Outline each uninfected red blood cell.
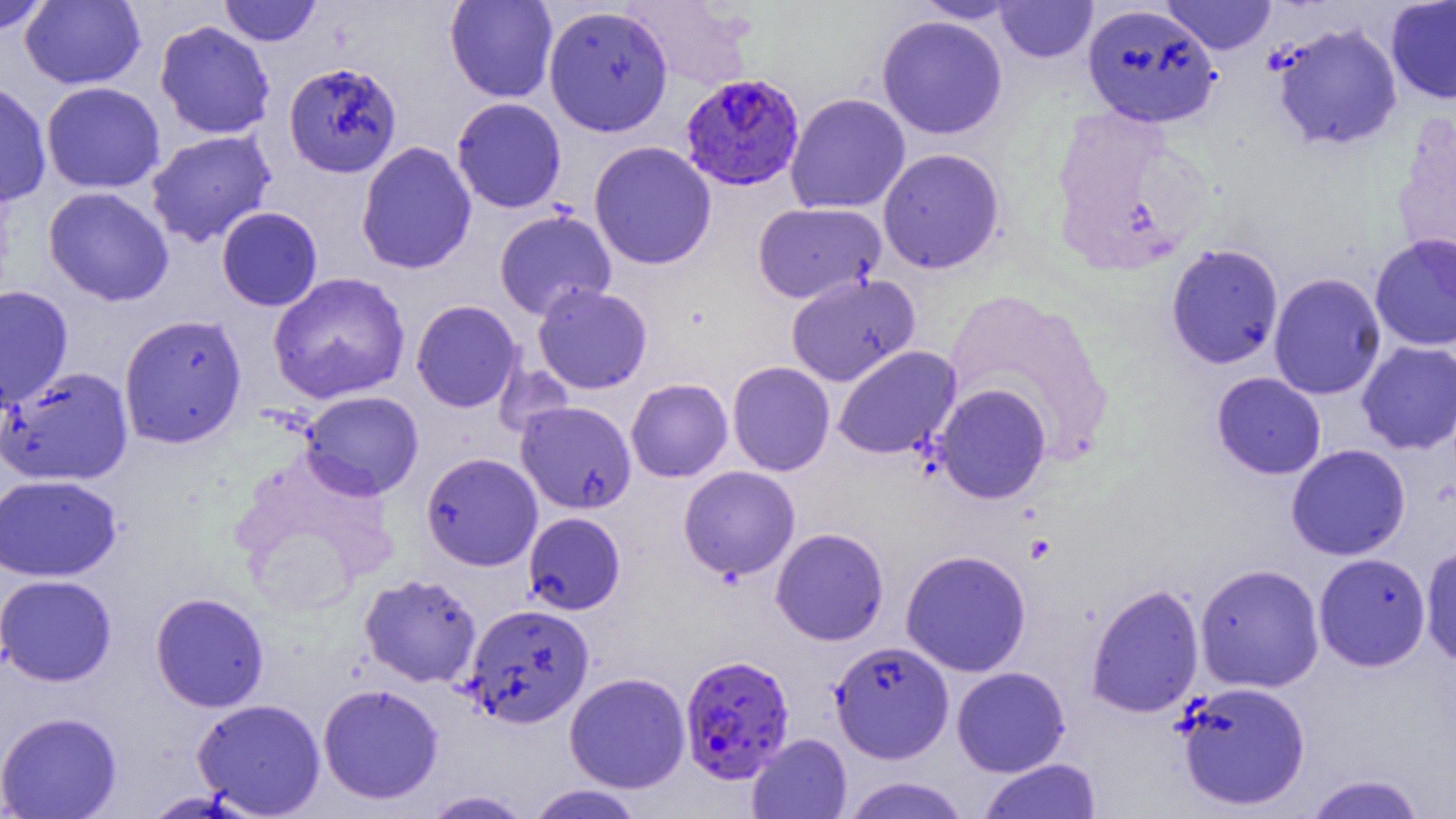
Approximate bounding boxes as [x1, y1, x2, y2] in pixels.
Uninfected red blood cells: [0, 0, 53, 36], [219, 0, 322, 46], [444, 0, 558, 103], [623, 0, 757, 92], [1161, 0, 1277, 55], [1385, 0, 1456, 105], [20, 1, 145, 89], [913, 1, 1023, 23], [994, 1, 1098, 63], [1082, 4, 1220, 128], [543, 5, 673, 137], [877, 15, 1008, 140], [154, 20, 275, 140], [1271, 23, 1403, 151], [283, 62, 403, 178], [0, 79, 52, 206], [41, 81, 165, 194], [785, 93, 910, 214], [451, 97, 567, 213], [1392, 115, 1456, 274], [146, 130, 277, 247], [356, 141, 477, 275], [589, 141, 716, 270], [878, 148, 1005, 274], [43, 187, 174, 306], [752, 201, 885, 303], [216, 207, 322, 311], [494, 209, 616, 321], [1369, 232, 1456, 351], [1165, 243, 1284, 370], [268, 272, 411, 404], [786, 272, 920, 386], [1268, 273, 1386, 400], [532, 283, 652, 394], [0, 285, 73, 410], [942, 288, 1115, 467], [411, 300, 523, 413], [119, 314, 247, 448], [1356, 341, 1456, 454], [833, 346, 962, 459], [727, 361, 835, 476], [0, 366, 133, 486], [1211, 372, 1327, 480], [626, 378, 732, 482], [933, 383, 1051, 504], [301, 390, 423, 500], [516, 401, 637, 514], [1286, 444, 1411, 561], [230, 449, 400, 611], [421, 452, 543, 571], [678, 465, 800, 581], [0, 474, 122, 581], [523, 512, 625, 615], [771, 527, 889, 646], [1420, 543, 1456, 667], [900, 549, 1031, 677], [1314, 553, 1431, 671], [1194, 563, 1324, 693], [0, 574, 117, 687], [359, 574, 482, 687], [1085, 583, 1204, 719], [150, 592, 269, 712], [464, 604, 595, 728], [829, 641, 954, 763], [951, 666, 1070, 776], [564, 672, 690, 793], [1175, 680, 1311, 811], [318, 683, 443, 804], [192, 698, 326, 817], [0, 711, 122, 818], [747, 733, 852, 818], [978, 758, 1102, 819], [1301, 773, 1428, 818], [840, 776, 971, 819], [526, 784, 645, 819], [420, 789, 534, 818].

slide_level_diagnosis: Plasmodium falciparum
magnification: 1000x
field_of_view: single
preparation: thin blood smear
plasmodium_falciparum_infected_red_blood_cell_locations: 'approximate bounding boxes as [x1, y1, x2, y2] in pixels: [680, 73, 805, 191], [680, 654, 794, 784]'
modality: optical microscopy
image_size: 1456×819 pixels